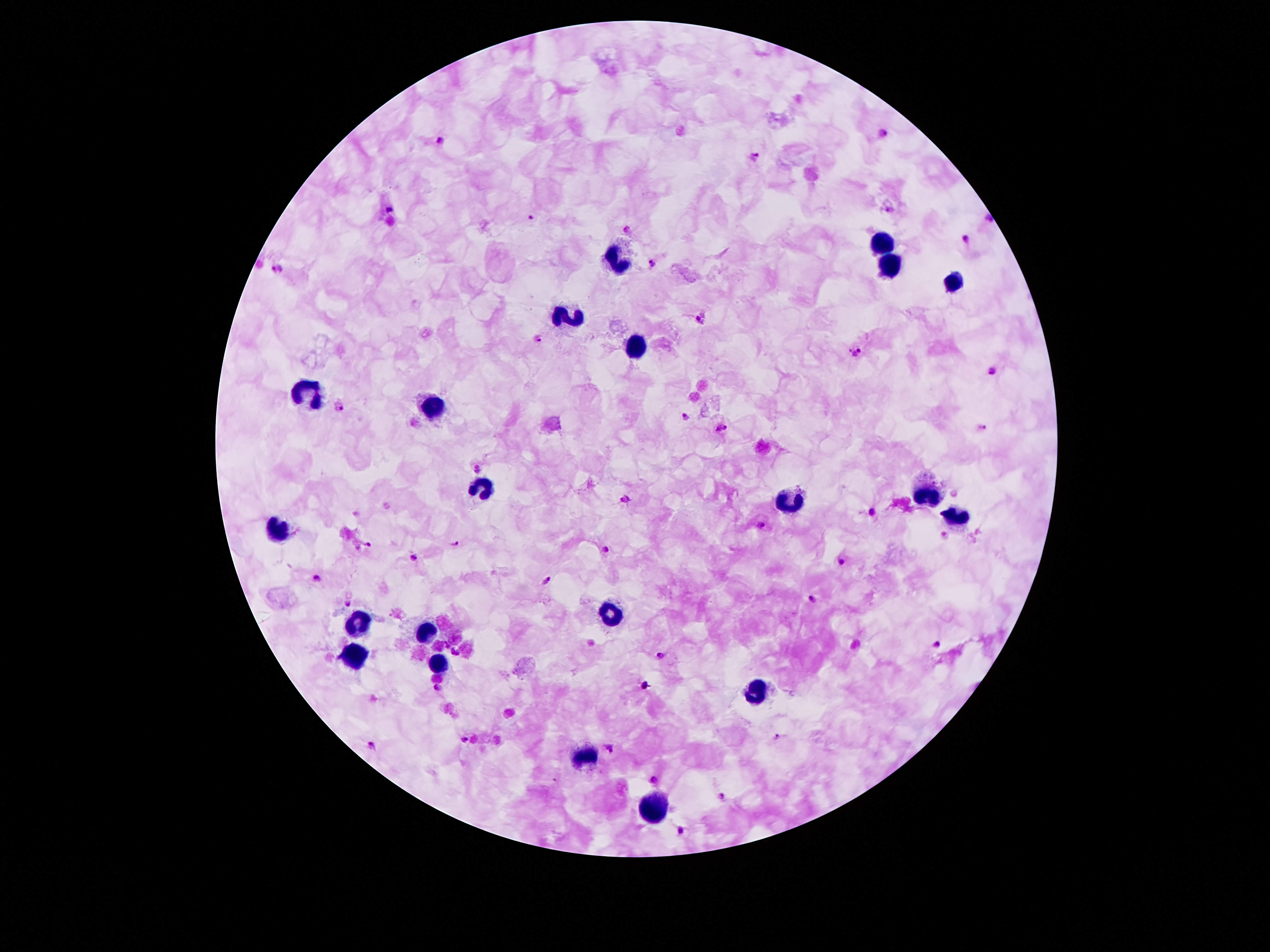
preparation: thick blood film
magnification: 100x
plasmodium_parasite_locations: 'approximate centers as (x, y) in pixels: (884, 133), (441, 139), (754, 157), (391, 208), (531, 217), (988, 219), (629, 231), (967, 241), (652, 261), (276, 268), (701, 320), (537, 338), (856, 351), (993, 370), (340, 404), (680, 418), (982, 426), (722, 427), (479, 466), (627, 501), (873, 512), (762, 524), (944, 538), (369, 543), (453, 543), (603, 548), (413, 556), (842, 561), (317, 578), (547, 579), (810, 598), (347, 601), (937, 645), (457, 654), (660, 655), (647, 685), (439, 687), (373, 744), (610, 747), (653, 780), (725, 795), (679, 830)'
field_of_view: one from this slide
stain: Giemsa
capture: smartphone camera through the microscope eyepiece
leukocyte_locations: 'approximate centers as (x, y) in pixels: (886, 245), (620, 257), (890, 264), (950, 282), (572, 318), (635, 345), (309, 389), (434, 404), (481, 487), (923, 495), (789, 503), (959, 516), (276, 530), (612, 612), (361, 620), (428, 631), (357, 652), (441, 662), (759, 689), (584, 758), (652, 809)'
image_size: 1270×952 pixels
patient_malaria_status: positive for Plasmodium falciparum